Identify the blood parasite species.
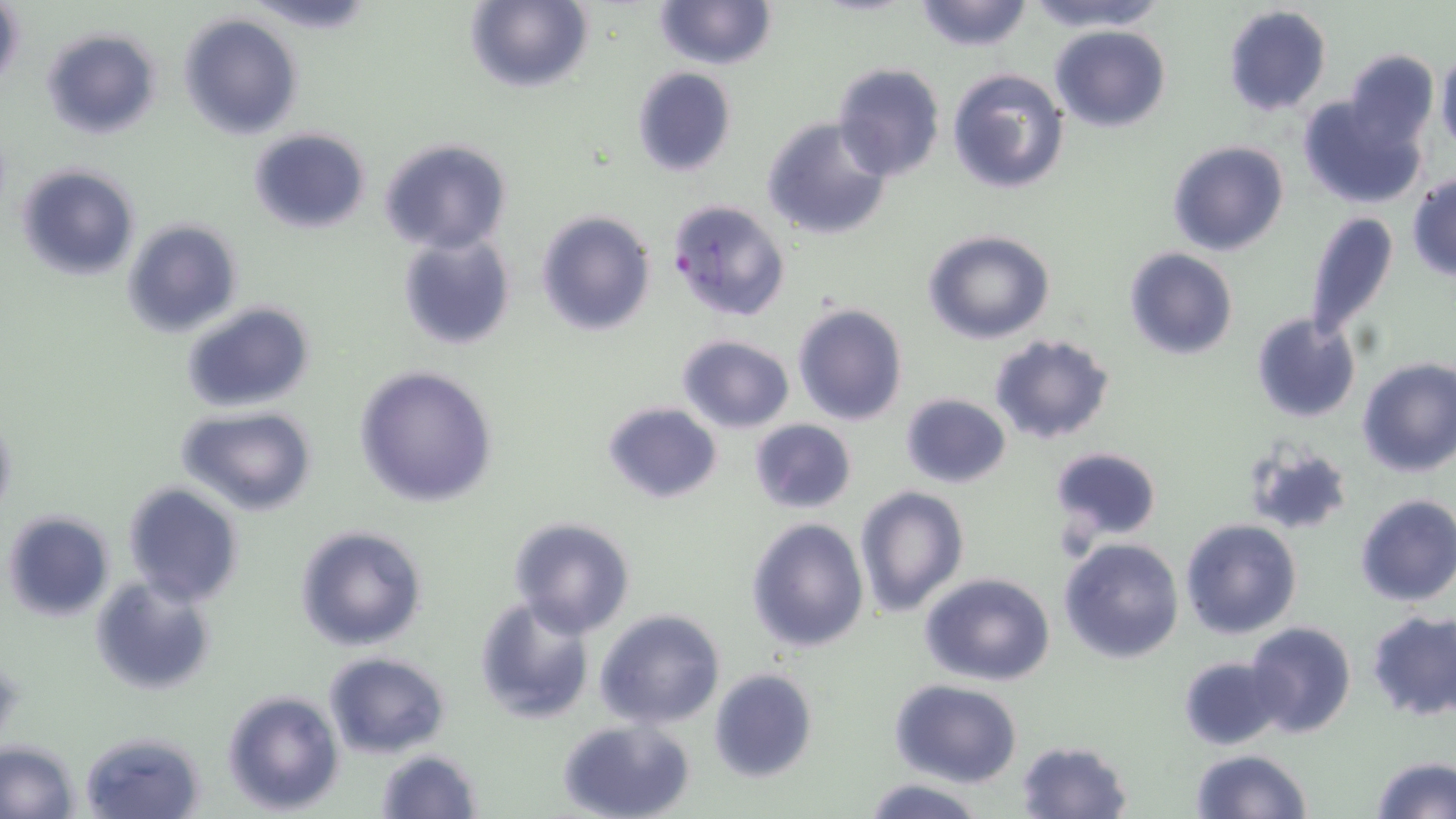
Plasmodium falciparum.

Approximate bounding boxes as named x1/y1/x2/y2 corners in pixels. Uninfected red blood cell locations: (x1=248, y1=0, x2=378, y2=34), (x1=464, y1=0, x2=592, y2=93), (x1=912, y1=0, x2=1036, y2=52), (x1=1025, y1=0, x2=1165, y2=31), (x1=656, y1=1, x2=776, y2=70), (x1=1, y1=3, x2=24, y2=96), (x1=1223, y1=5, x2=1331, y2=117), (x1=179, y1=13, x2=303, y2=140), (x1=1049, y1=25, x2=1172, y2=131), (x1=41, y1=28, x2=162, y2=141), (x1=1339, y1=49, x2=1440, y2=151), (x1=1436, y1=50, x2=1456, y2=152), (x1=831, y1=63, x2=945, y2=181), (x1=631, y1=67, x2=737, y2=178), (x1=946, y1=68, x2=1068, y2=194), (x1=1298, y1=94, x2=1425, y2=209), (x1=761, y1=116, x2=893, y2=241), (x1=248, y1=127, x2=370, y2=234), (x1=379, y1=137, x2=512, y2=255), (x1=1167, y1=140, x2=1289, y2=256), (x1=15, y1=163, x2=141, y2=282), (x1=1408, y1=174, x2=1456, y2=282), (x1=536, y1=209, x2=655, y2=336), (x1=1303, y1=209, x2=1400, y2=347), (x1=121, y1=219, x2=243, y2=338), (x1=923, y1=230, x2=1055, y2=344), (x1=398, y1=235, x2=516, y2=351), (x1=1124, y1=247, x2=1238, y2=361), (x1=181, y1=301, x2=315, y2=412), (x1=792, y1=304, x2=908, y2=426), (x1=1250, y1=313, x2=1360, y2=424), (x1=988, y1=333, x2=1115, y2=446), (x1=676, y1=334, x2=795, y2=432), (x1=1357, y1=358, x2=1456, y2=477), (x1=353, y1=364, x2=500, y2=507), (x1=899, y1=393, x2=1011, y2=487), (x1=601, y1=400, x2=724, y2=505), (x1=176, y1=405, x2=318, y2=516), (x1=0, y1=410, x2=16, y2=524), (x1=748, y1=418, x2=857, y2=514), (x1=1241, y1=440, x2=1355, y2=539), (x1=1049, y1=446, x2=1163, y2=545), (x1=123, y1=483, x2=243, y2=607), (x1=853, y1=485, x2=969, y2=616), (x1=1355, y1=495, x2=1456, y2=607), (x1=3, y1=511, x2=114, y2=622), (x1=746, y1=516, x2=869, y2=653), (x1=507, y1=517, x2=637, y2=638), (x1=1180, y1=518, x2=1302, y2=640), (x1=294, y1=524, x2=428, y2=652), (x1=1058, y1=537, x2=1184, y2=663), (x1=919, y1=571, x2=1058, y2=687), (x1=89, y1=577, x2=217, y2=697), (x1=473, y1=596, x2=596, y2=724), (x1=594, y1=608, x2=727, y2=729), (x1=1366, y1=609, x2=1456, y2=722), (x1=1244, y1=620, x2=1357, y2=738), (x1=323, y1=652, x2=450, y2=758), (x1=1178, y1=656, x2=1286, y2=750), (x1=708, y1=668, x2=818, y2=783), (x1=888, y1=679, x2=1025, y2=786), (x1=221, y1=690, x2=343, y2=813), (x1=557, y1=716, x2=697, y2=819), (x1=79, y1=731, x2=205, y2=819), (x1=1015, y1=740, x2=1132, y2=819), (x1=0, y1=743, x2=79, y2=817), (x1=1188, y1=748, x2=1311, y2=819), (x1=374, y1=749, x2=481, y2=819), (x1=1369, y1=756, x2=1456, y2=818), (x1=862, y1=778, x2=986, y2=817). Plasmodium falciparum-infected red blood cell locations: (x1=666, y1=197, x2=792, y2=325). One field of a larger specimen. May-Grünwald-Giemsa stain. Image is 1456×819 pixels. 1000x magnification. Thin blood smear. Light microscopy.